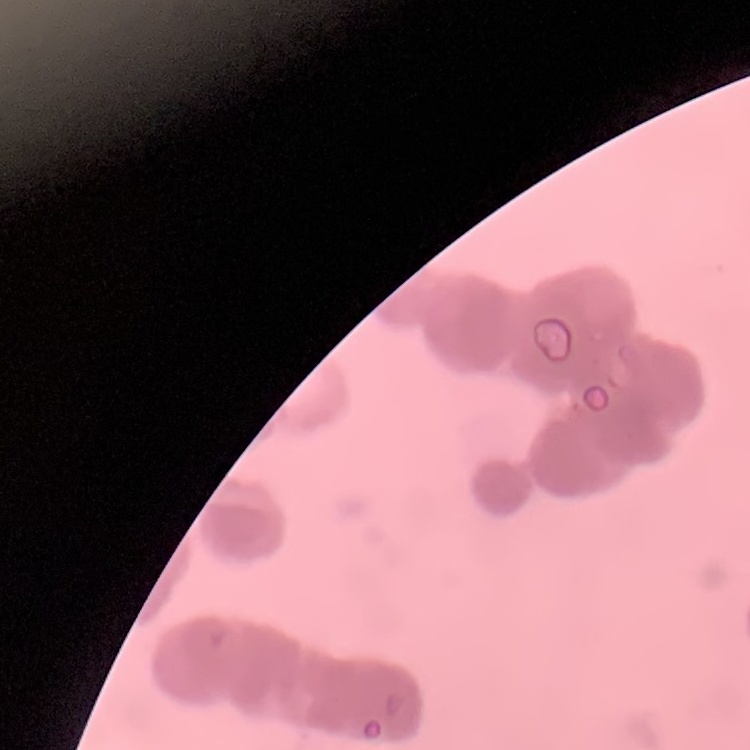
Summary:
  - Red blood cell morphology: rouleaux formation
  - Stain: Field's or Giemsa
  - Image type: square crop of a larger photomicrograph
  - Preparation: thin peripheral smear